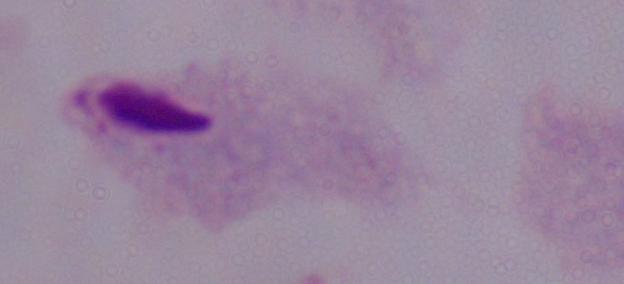

Summary:
  - Magnification: 1000x
  - Identification: trichomonad
  - Modality: micrograph